Report the malaria status of this cell.
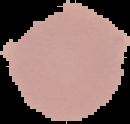
Uninfected.

Summary:
  - Preparation: thin blood smear
  - Image type: segmented cell region on a black background
  - Image size: 130×124 pixels